Assess the morphology of the red blood cells.
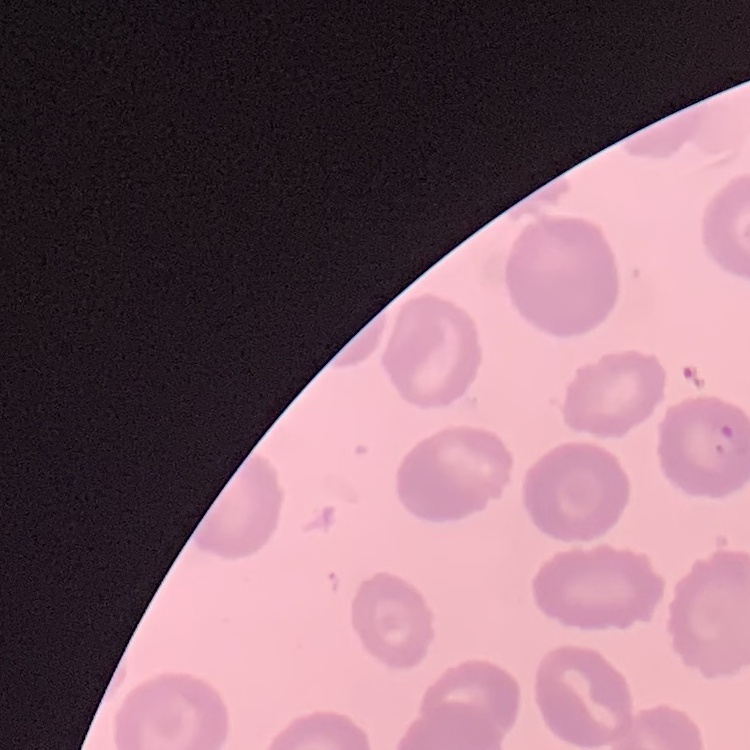

No rouleaux formation.

Summary:
  - Stain: Field's or Giemsa
  - Image type: one tile cut from a larger photomicrograph
  - Preparation: thin blood film